Report the malaria status of this cell.
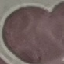
Uninfected.

capture: smartphone camera at the microscope eyepiece
image_type: automatically extracted cell patch, resized to 64 × 64 pixels
preparation: thin smear
stain: Giemsa